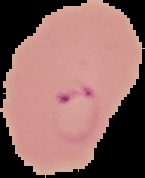

Summary:
  - Preparation: thin blood film
  - Malaria status: parasitized
  - Image size: 145×178 pixels
  - Image type: segmented cell region with the area outside set to black